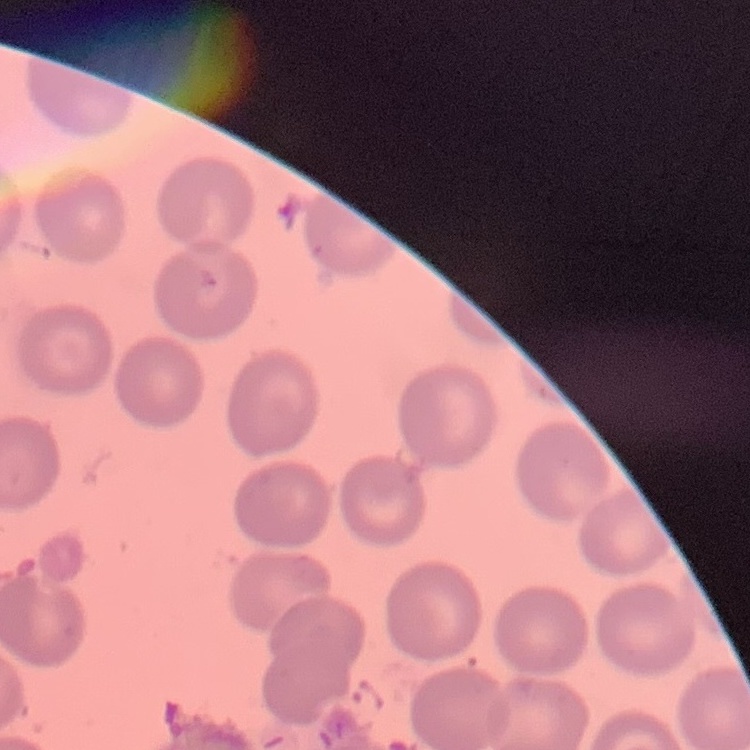

The erythrocytes show no rouleaux formation. Stained with either Field's or Giemsa. One tile cut from a larger photomicrograph. Thin blood smear.